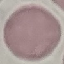
Summary:
  - Result: negative for malaria parasites
  - Image type: automatically extracted cell patch, resized to 64 × 64 pixels
  - Capture: smartphone through the microscope eyepiece
  - Preparation: thin blood film
  - Stain: Giemsa